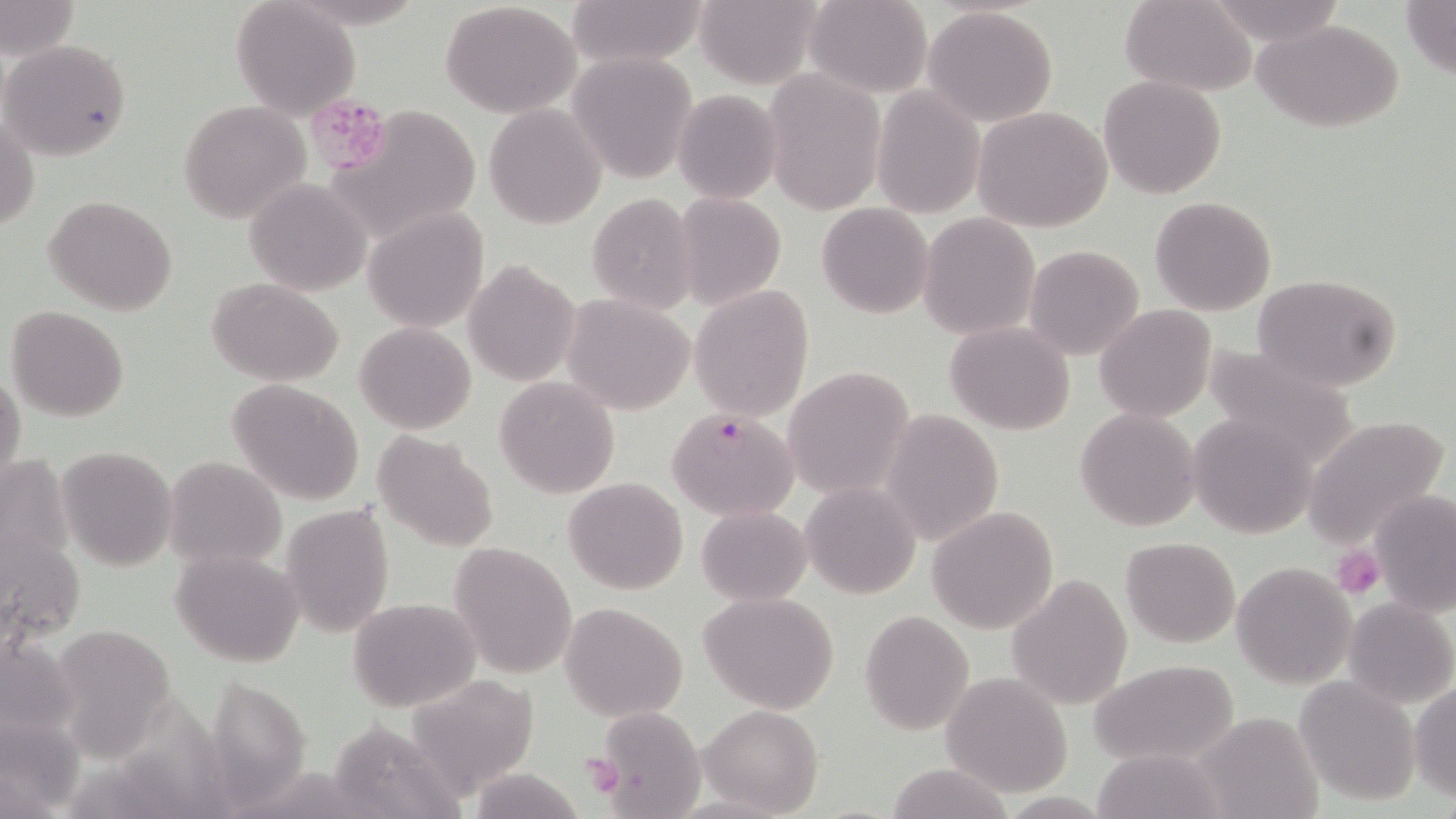
Approximate bounding boxes as [x1, y1, x2, y2] in pixels. Platelet locations: [326, 99, 485, 243], [1331, 547, 1385, 600], [579, 752, 624, 799]. Uninfected red blood cell locations: [566, 0, 708, 70], [693, 0, 821, 90], [803, 0, 933, 98], [1120, 0, 1254, 95], [0, 1, 78, 64], [230, 1, 361, 122], [439, 1, 581, 116], [1202, 1, 1347, 45], [1401, 1, 1456, 80], [921, 6, 1060, 128], [1256, 19, 1403, 132], [1, 38, 132, 161], [566, 51, 699, 184], [762, 71, 885, 215], [1098, 75, 1227, 198], [871, 86, 984, 218], [673, 89, 783, 204], [320, 100, 390, 174], [178, 101, 310, 224], [483, 103, 607, 229], [973, 106, 1112, 231], [1, 110, 38, 237], [244, 178, 370, 296], [674, 190, 787, 311], [586, 192, 699, 313], [45, 195, 178, 316], [1150, 196, 1275, 315], [816, 202, 934, 318], [365, 210, 488, 332], [918, 212, 1040, 341], [1025, 245, 1146, 361], [464, 259, 580, 386], [1253, 274, 1402, 392], [208, 278, 345, 386], [688, 286, 815, 422], [562, 294, 696, 416], [1094, 304, 1216, 421], [6, 305, 129, 422], [354, 321, 475, 434], [945, 322, 1075, 435], [1202, 342, 1361, 472], [783, 367, 915, 497], [0, 368, 26, 496], [494, 376, 619, 497], [227, 378, 366, 504], [1075, 408, 1201, 531], [881, 409, 1005, 545], [1187, 410, 1320, 539], [1302, 416, 1450, 548], [372, 431, 498, 553], [57, 445, 178, 569], [164, 455, 287, 572], [0, 456, 77, 596], [563, 477, 689, 593], [800, 480, 921, 600], [1368, 490, 1456, 617], [279, 502, 395, 639], [926, 505, 1058, 634], [696, 506, 811, 605], [0, 513, 85, 652], [1120, 536, 1240, 647], [449, 541, 579, 678], [171, 548, 305, 668], [1230, 560, 1358, 689], [1006, 572, 1132, 710], [699, 591, 841, 714], [1342, 597, 1454, 710], [348, 598, 479, 712], [560, 601, 687, 721], [859, 611, 974, 733], [47, 622, 181, 757], [0, 632, 80, 741], [1087, 659, 1239, 768], [940, 673, 1073, 798], [220, 676, 314, 803], [408, 676, 541, 800], [1293, 676, 1421, 805], [1410, 682, 1456, 801], [147, 694, 235, 819], [698, 705, 824, 818], [590, 706, 704, 817], [1193, 711, 1322, 819], [0, 716, 87, 815], [321, 718, 462, 819], [1090, 747, 1226, 819], [885, 763, 1017, 819]. Plasmodium falciparum-infected red blood cell locations: [667, 408, 800, 521]. Slide-level diagnosis: Plasmodium falciparum. May-Grünwald-Giemsa stain. Thin blood film. Optical microscopy. One field of a larger specimen. 1000x magnification. Image is 1456×819 pixels.